Locate every Plasmodium falciparum-infected red blood cell.
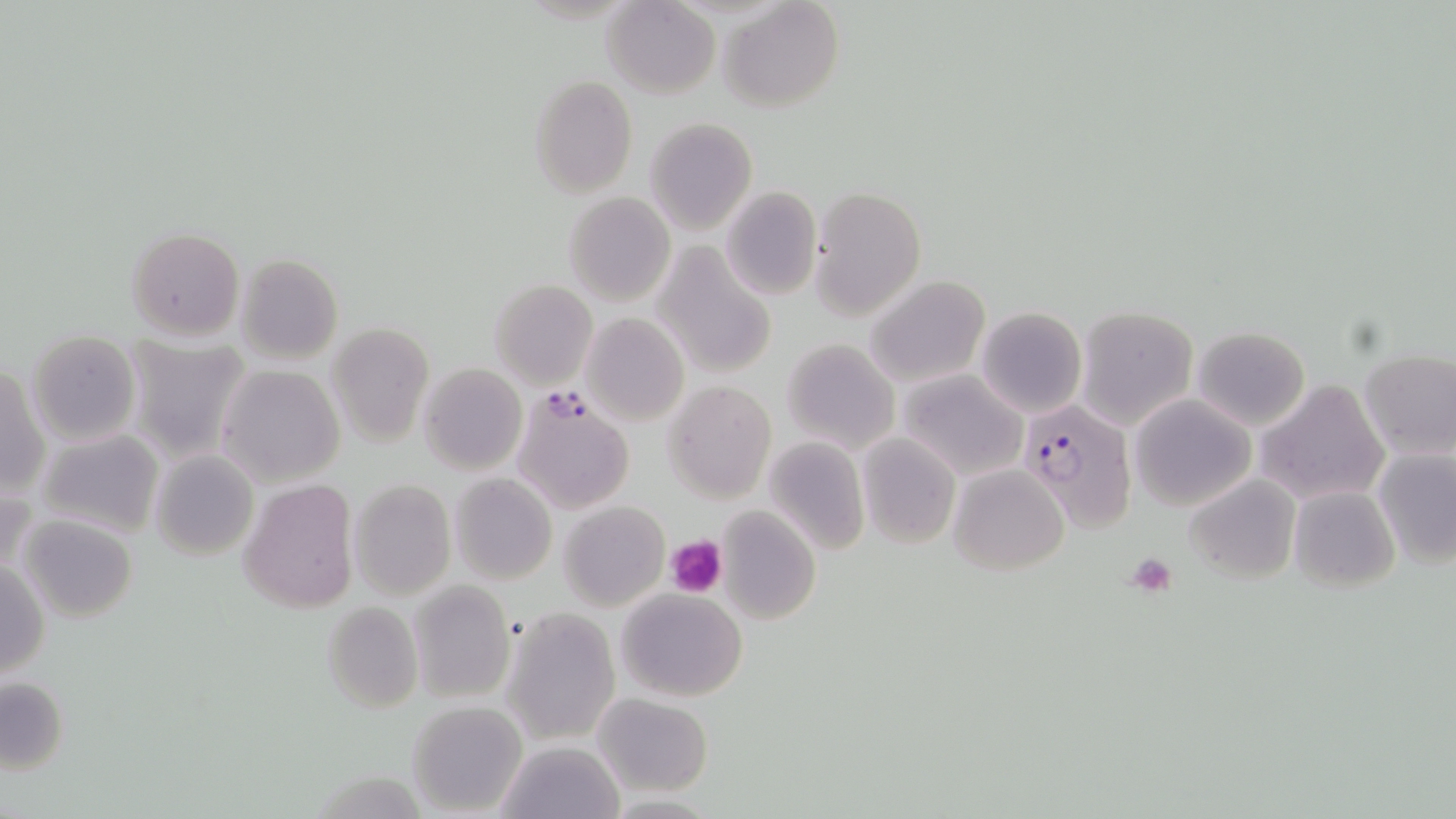

Approximate bounding boxes as [x1, y1, x2, y2] in pixels.
Plasmodium falciparum-infected red blood cells: [512, 393, 636, 517], [1017, 399, 1138, 534].

Uninfected red blood cell locations: [603, 0, 720, 99], [720, 0, 843, 113], [528, 74, 639, 197], [645, 117, 757, 236], [719, 186, 821, 300], [808, 186, 925, 321], [563, 191, 677, 308], [126, 227, 245, 342], [653, 244, 777, 381], [236, 254, 343, 365], [865, 276, 991, 389], [489, 279, 597, 390], [976, 306, 1086, 416], [1076, 307, 1197, 429], [579, 314, 688, 425], [328, 322, 433, 447], [1192, 326, 1309, 431], [26, 330, 140, 445], [123, 336, 252, 463], [781, 337, 900, 455], [1359, 350, 1456, 461], [418, 363, 526, 476], [1, 365, 47, 499], [218, 365, 346, 487], [896, 369, 1028, 482], [1256, 380, 1389, 505], [663, 382, 776, 503], [1130, 394, 1255, 512], [874, 396, 1004, 524], [37, 429, 165, 541], [856, 432, 960, 549], [762, 437, 871, 555], [1374, 448, 1456, 568], [150, 449, 259, 561], [950, 464, 1069, 574], [449, 473, 556, 585], [1185, 474, 1301, 585], [237, 477, 360, 613], [348, 479, 456, 599], [1287, 485, 1399, 593], [559, 502, 669, 612], [717, 506, 821, 625], [15, 514, 139, 623], [0, 559, 49, 678], [409, 581, 513, 702], [616, 587, 749, 701], [322, 602, 423, 713], [503, 608, 619, 746], [0, 676, 68, 773], [592, 693, 713, 798], [405, 701, 526, 816], [497, 741, 624, 819], [601, 794, 725, 818]. Platelet locations: [667, 534, 727, 599], [1124, 552, 1176, 595]. Slide-level diagnosis: Plasmodium falciparum. Image is 1456×819 pixels. May-Grünwald-Giemsa stain. 1000x magnification. One field of a larger specimen. Light microscopy. Thin blood film.